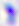

Toxoplasma gondii is shown. 400x magnification. Photomicrograph.